Classify this cell by malaria status.
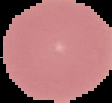
It is uninfected.

Image is 112×103 pixels. From a thin blood film. Segmented cell region on a black background.